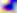

Summary:
  - Modality: micrograph
  - Magnification: 400x
  - Identification: Toxoplasma gondii